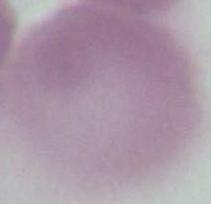

Summary:
  - Magnification: 1000x
  - Modality: micrograph
  - Identification: erythrocyte